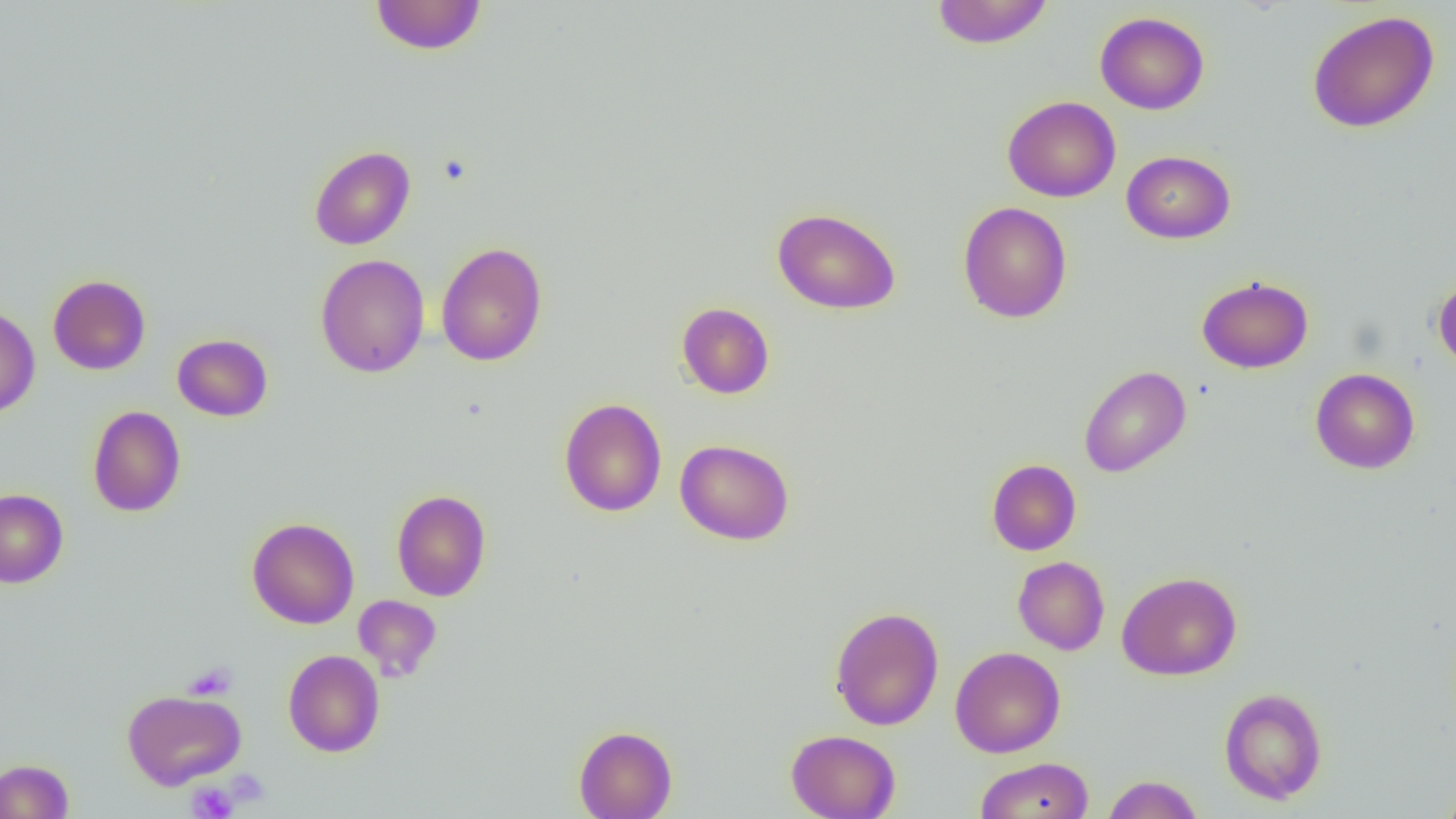

{
  "slide_level_diagnosis": "no evidence of blood parasites",
  "uninfected_red_blood_cell_locations": "approximate bounding boxes as named x1/y1/x2/y2 corners in pixels: (x1=370, y1=0, x2=487, y2=56), (x1=930, y1=0, x2=1053, y2=49), (x1=1095, y1=11, x2=1209, y2=114), (x1=1306, y1=11, x2=1440, y2=133), (x1=1002, y1=96, x2=1121, y2=202), (x1=309, y1=145, x2=415, y2=250), (x1=1121, y1=150, x2=1235, y2=243), (x1=958, y1=202, x2=1073, y2=323), (x1=772, y1=207, x2=901, y2=315), (x1=435, y1=241, x2=548, y2=366), (x1=315, y1=253, x2=430, y2=378), (x1=48, y1=274, x2=151, y2=375), (x1=1433, y1=274, x2=1456, y2=371), (x1=1197, y1=275, x2=1313, y2=374), (x1=676, y1=302, x2=775, y2=399), (x1=0, y1=305, x2=40, y2=418), (x1=172, y1=334, x2=273, y2=421), (x1=1079, y1=365, x2=1191, y2=477), (x1=1310, y1=367, x2=1420, y2=474), (x1=559, y1=398, x2=667, y2=517), (x1=87, y1=405, x2=186, y2=517), (x1=675, y1=439, x2=795, y2=545), (x1=986, y1=458, x2=1082, y2=556), (x1=0, y1=489, x2=68, y2=588), (x1=391, y1=489, x2=491, y2=601), (x1=247, y1=517, x2=359, y2=629), (x1=1012, y1=556, x2=1110, y2=655), (x1=1117, y1=571, x2=1242, y2=680), (x1=353, y1=595, x2=442, y2=680), (x1=828, y1=606, x2=944, y2=731), (x1=950, y1=646, x2=1065, y2=758), (x1=283, y1=649, x2=385, y2=757), (x1=1219, y1=687, x2=1327, y2=804), (x1=121, y1=688, x2=246, y2=790), (x1=574, y1=725, x2=677, y2=819), (x1=786, y1=729, x2=901, y2=819), (x1=975, y1=757, x2=1094, y2=819), (x1=0, y1=759, x2=73, y2=818), (x1=1102, y1=774, x2=1204, y2=818), (x1=1440, y1=778, x2=1456, y2=819)",
  "image_size": "1456×819 pixels",
  "magnification": "1000x",
  "field_of_view": "single",
  "platelet_locations": "approximate bounding boxes as named x1/y1/x2/y2 corners in pixels: (x1=184, y1=662, x2=238, y2=700), (x1=187, y1=782, x2=239, y2=819)",
  "modality": "light microscopy",
  "preparation": "thin blood film"
}